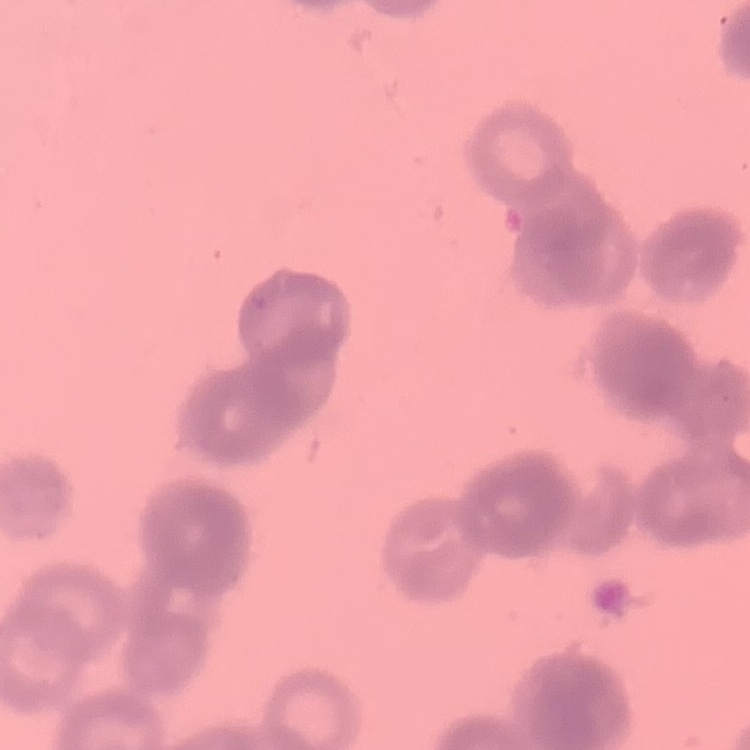

erythrocyte_morphology: rouleaux formation
stain: Field's or Giemsa
image_type: one tile cut from a larger photomicrograph
preparation: thin blood smear